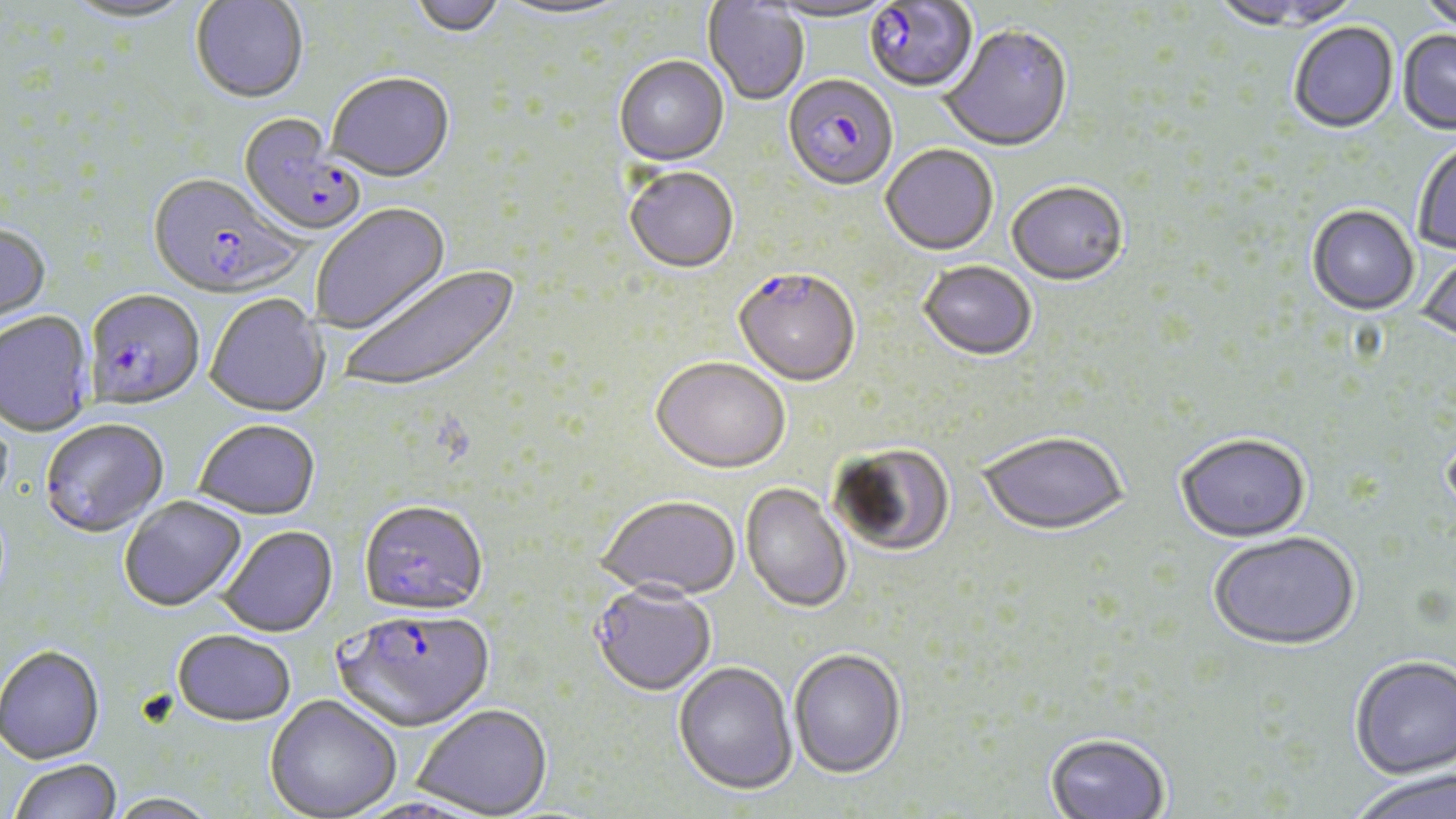
slide-level diagnosis = Plasmodium falciparum
stain = May-Grünwald-Giemsa
uninfected red blood cell locations = approximate bounding boxes as named x1/y1/x2/y2 corners in pixels: (x1=61, y1=0, x2=197, y2=27), (x1=408, y1=0, x2=506, y2=39), (x1=765, y1=0, x2=897, y2=25), (x1=1418, y1=0, x2=1456, y2=36), (x1=190, y1=1, x2=308, y2=106), (x1=493, y1=1, x2=631, y2=23), (x1=702, y1=1, x2=809, y2=107), (x1=1207, y1=1, x2=1353, y2=33), (x1=1289, y1=23, x2=1399, y2=135), (x1=939, y1=27, x2=1074, y2=155), (x1=1397, y1=31, x2=1456, y2=137), (x1=614, y1=57, x2=729, y2=167), (x1=327, y1=75, x2=455, y2=185), (x1=1413, y1=140, x2=1456, y2=257), (x1=881, y1=146, x2=998, y2=258), (x1=624, y1=169, x2=739, y2=275), (x1=1006, y1=184, x2=1129, y2=288), (x1=312, y1=204, x2=452, y2=335), (x1=1307, y1=207, x2=1419, y2=318), (x1=0, y1=226, x2=52, y2=337), (x1=1417, y1=253, x2=1456, y2=350), (x1=918, y1=263, x2=1037, y2=363), (x1=339, y1=265, x2=522, y2=396), (x1=204, y1=295, x2=330, y2=420), (x1=0, y1=312, x2=95, y2=438), (x1=651, y1=360, x2=790, y2=477), (x1=194, y1=421, x2=321, y2=523), (x1=978, y1=435, x2=1128, y2=539), (x1=1175, y1=436, x2=1312, y2=545), (x1=830, y1=444, x2=956, y2=558), (x1=741, y1=484, x2=852, y2=614), (x1=119, y1=498, x2=247, y2=615), (x1=597, y1=498, x2=741, y2=603), (x1=219, y1=527, x2=339, y2=639), (x1=1209, y1=534, x2=1361, y2=654), (x1=589, y1=586, x2=717, y2=698), (x1=172, y1=632, x2=296, y2=730), (x1=0, y1=647, x2=105, y2=766), (x1=789, y1=650, x2=906, y2=780), (x1=1349, y1=658, x2=1456, y2=783), (x1=673, y1=663, x2=797, y2=797), (x1=264, y1=696, x2=401, y2=819), (x1=412, y1=706, x2=553, y2=818), (x1=1044, y1=735, x2=1171, y2=819), (x1=10, y1=761, x2=122, y2=819), (x1=1347, y1=773, x2=1456, y2=819), (x1=103, y1=794, x2=222, y2=819)
preparation = thin blood smear
magnification = 1000x
modality = light microscopy
Plasmodium falciparum-infected red blood cell locations = approximate bounding boxes as named x1/y1/x2/y2 corners in pixels: (x1=863, y1=1, x2=978, y2=96), (x1=783, y1=75, x2=898, y2=193), (x1=237, y1=115, x2=366, y2=239), (x1=147, y1=175, x2=305, y2=302), (x1=732, y1=272, x2=861, y2=389), (x1=84, y1=292, x2=205, y2=412), (x1=40, y1=421, x2=169, y2=540), (x1=358, y1=503, x2=488, y2=620), (x1=334, y1=611, x2=496, y2=734)
image size = 1456×819 pixels
field of view = single